Outline each Plasmodium malariae-infected red blood cell.
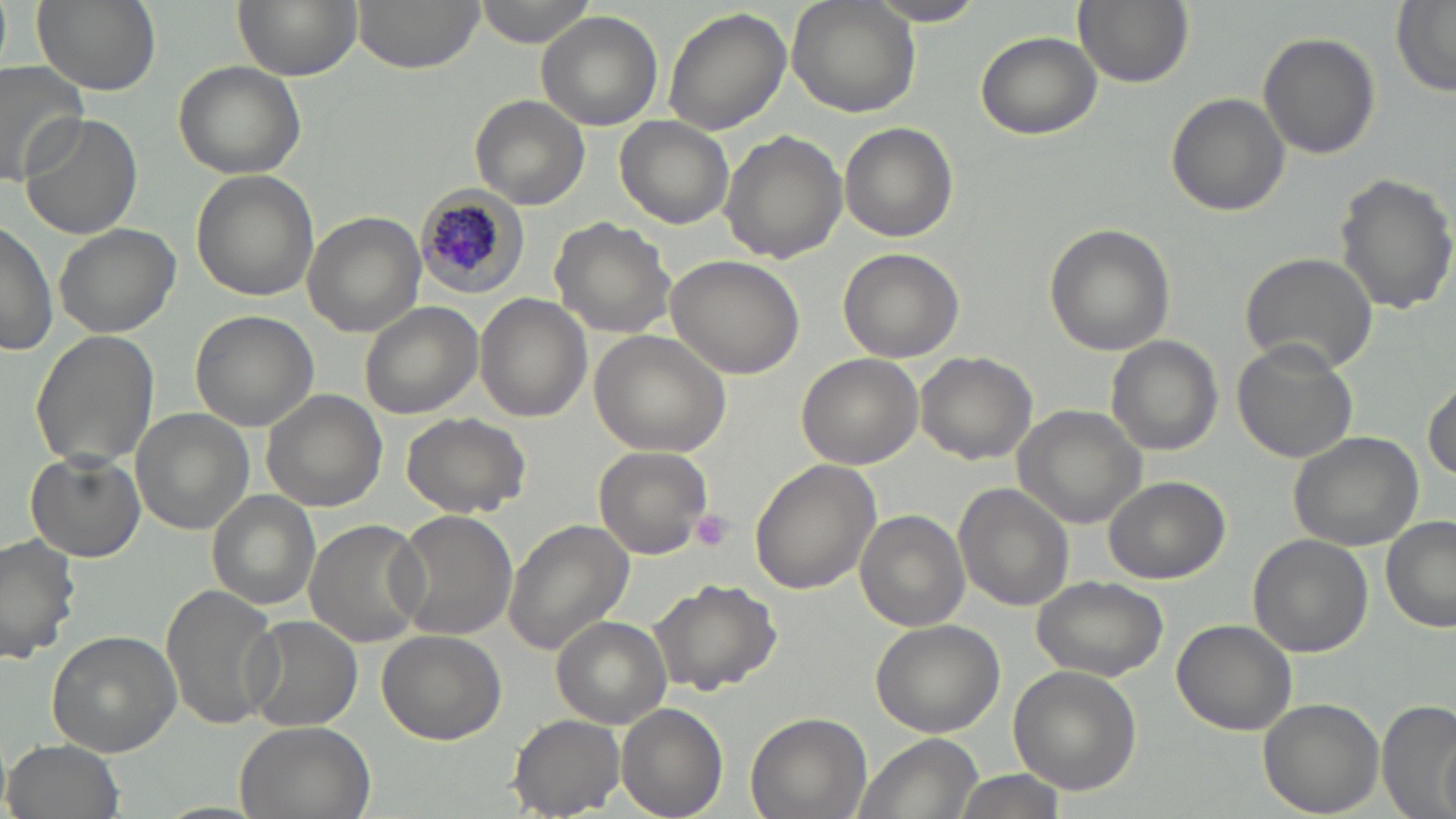

Approximate bounding boxes as (x1, y1, x2, y2) in pixels.
Plasmodium malariae-infected red blood cells: (415, 188, 533, 297).

{
  "slide_level_diagnosis": "Plasmodium malariae",
  "platelet_locations": "approximate bounding boxes as (x1, y1, x2, y2) in pixels: (690, 509, 734, 553)",
  "magnification": "1000x",
  "modality": "optical microscopy",
  "preparation": "thin blood film",
  "image_size": "1456×819 pixels",
  "field_of_view": "one of a larger specimen",
  "uninfected_red_blood_cell_locations": "approximate bounding boxes as (x1, y1, x2, y2) in pixels: (30, 0, 162, 96), (232, 0, 362, 79), (352, 0, 480, 73), (474, 0, 596, 47), (786, 0, 921, 119), (864, 0, 989, 27), (1073, 0, 1193, 89), (1391, 1, 1456, 95), (661, 6, 792, 136), (535, 11, 661, 130), (975, 31, 1101, 140), (1259, 31, 1380, 160), (173, 60, 306, 179), (0, 63, 93, 187), (1167, 92, 1289, 216), (470, 96, 591, 210), (18, 113, 144, 242), (614, 115, 733, 228), (841, 122, 956, 243), (720, 131, 847, 265), (190, 171, 318, 300), (1334, 174, 1456, 317), (301, 211, 426, 335), (550, 215, 679, 338), (0, 220, 57, 356), (53, 222, 181, 338), (1042, 222, 1176, 358), (838, 247, 964, 362), (1238, 250, 1380, 375), (666, 252, 806, 381), (476, 294, 589, 422), (359, 302, 484, 419), (189, 312, 318, 431), (31, 329, 159, 470), (589, 329, 733, 457), (1104, 337, 1223, 456), (1232, 341, 1359, 464), (914, 349, 1037, 464), (796, 354, 923, 469), (1425, 381, 1456, 480), (260, 389, 387, 513), (1016, 405, 1151, 530), (132, 408, 254, 535), (400, 411, 531, 520), (1288, 428, 1425, 551), (593, 445, 714, 560), (25, 451, 146, 563), (749, 460, 882, 597), (1103, 475, 1229, 584), (954, 483, 1074, 611), (206, 490, 321, 610), (389, 510, 520, 642), (855, 510, 970, 630), (1381, 516, 1456, 633), (304, 520, 429, 647), (505, 520, 634, 653), (0, 533, 81, 664), (1248, 534, 1373, 657), (1030, 576, 1170, 681), (649, 579, 781, 696), (160, 584, 282, 734), (242, 615, 362, 732), (552, 616, 672, 726), (869, 616, 1007, 736), (1172, 618, 1297, 734), (45, 630, 181, 757), (376, 630, 506, 744), (1010, 665, 1142, 795), (1257, 698, 1385, 819), (1377, 698, 1456, 819), (617, 702, 728, 819), (745, 711, 870, 819), (509, 714, 626, 816), (232, 719, 374, 819), (852, 733, 981, 819), (6, 737, 123, 819), (949, 770, 1062, 818)",
  "stain": "May-Grünwald-Giemsa"
}